Locate every Plasmodium vivax-infected red blood cell.
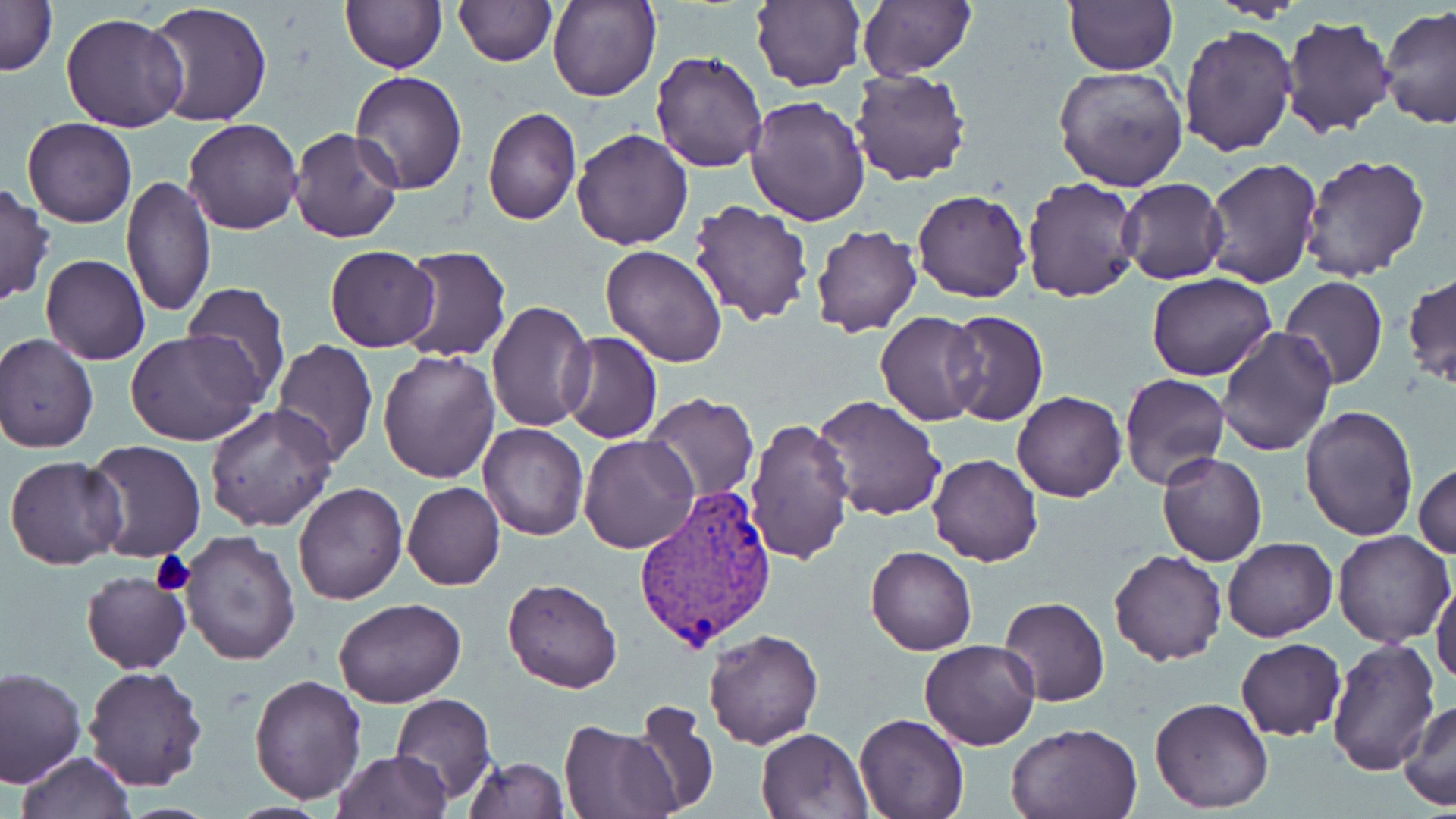

Approximate bounding boxes as (x1, y1, x2, y2) in pixels.
Plasmodium vivax-infected red blood cells: (634, 485, 778, 654).

slide-level diagnosis = Plasmodium vivax
modality = light microscopy
image size = 1456×819 pixels
magnification = 1000x
platelet locations = approximate bounding boxes as (x1, y1, x2, y2) in pixels: (149, 549, 196, 596)
preparation = thin blood film
field of view = single
uninfected red blood cell locations = approximate bounding boxes as (x1, y1, x2, y2) in pixels: (0, 0, 57, 76), (548, 0, 662, 102), (750, 0, 865, 90), (1065, 0, 1178, 75), (857, 1, 975, 78), (340, 2, 447, 73), (453, 2, 555, 67), (143, 3, 273, 128), (1378, 6, 1456, 128), (60, 13, 187, 133), (1278, 14, 1397, 139), (1178, 22, 1297, 158), (650, 49, 770, 172), (1054, 65, 1189, 191), (850, 69, 970, 185), (349, 70, 467, 193), (746, 95, 872, 228), (304, 99, 453, 224), (483, 106, 582, 226), (22, 117, 136, 228), (184, 118, 303, 235), (288, 127, 404, 245), (569, 128, 693, 249), (1299, 153, 1430, 283), (1204, 157, 1323, 289), (120, 176, 217, 320), (1022, 176, 1142, 303), (1119, 178, 1229, 285), (0, 184, 55, 306), (912, 188, 1029, 303), (687, 200, 814, 326), (811, 224, 923, 338), (325, 245, 439, 352), (601, 245, 728, 368), (397, 246, 511, 361), (40, 254, 150, 365), (1404, 269, 1454, 389), (1146, 272, 1276, 381), (1279, 276, 1389, 389), (180, 282, 292, 403), (485, 301, 593, 432), (942, 310, 1048, 426), (875, 311, 986, 426), (1217, 327, 1337, 457), (125, 329, 263, 446), (1, 332, 99, 452), (560, 332, 662, 444), (270, 338, 377, 467), (377, 348, 502, 483), (1119, 374, 1230, 491), (1012, 389, 1126, 502), (643, 392, 760, 503), (813, 394, 948, 522), (672, 401, 803, 550), (205, 403, 337, 533), (1299, 405, 1419, 542), (743, 416, 855, 565), (478, 423, 588, 541), (578, 433, 700, 554), (82, 440, 207, 562), (1157, 452, 1267, 567), (928, 454, 1042, 567), (5, 455, 127, 571), (1413, 461, 1456, 560), (293, 481, 408, 605), (402, 481, 506, 592), (178, 529, 302, 667), (1332, 529, 1454, 647), (1223, 537, 1337, 640), (866, 545, 977, 654), (1109, 548, 1227, 665), (79, 570, 192, 675), (502, 577, 622, 692), (1432, 579, 1456, 689), (998, 595, 1110, 706), (334, 598, 467, 708), (703, 628, 823, 749), (1326, 636, 1440, 777), (1236, 638, 1346, 741), (917, 640, 1039, 751), (82, 665, 208, 793), (0, 667, 84, 788), (250, 674, 366, 803), (390, 693, 495, 804), (1149, 696, 1274, 812), (625, 700, 720, 817), (1399, 700, 1456, 811), (854, 713, 969, 819), (558, 721, 680, 819), (1006, 722, 1143, 819), (756, 727, 873, 817), (332, 751, 450, 819), (16, 752, 135, 819), (465, 757, 571, 818)
stain = May-Grünwald-Giemsa